Comment on the morphology of the red blood cells.
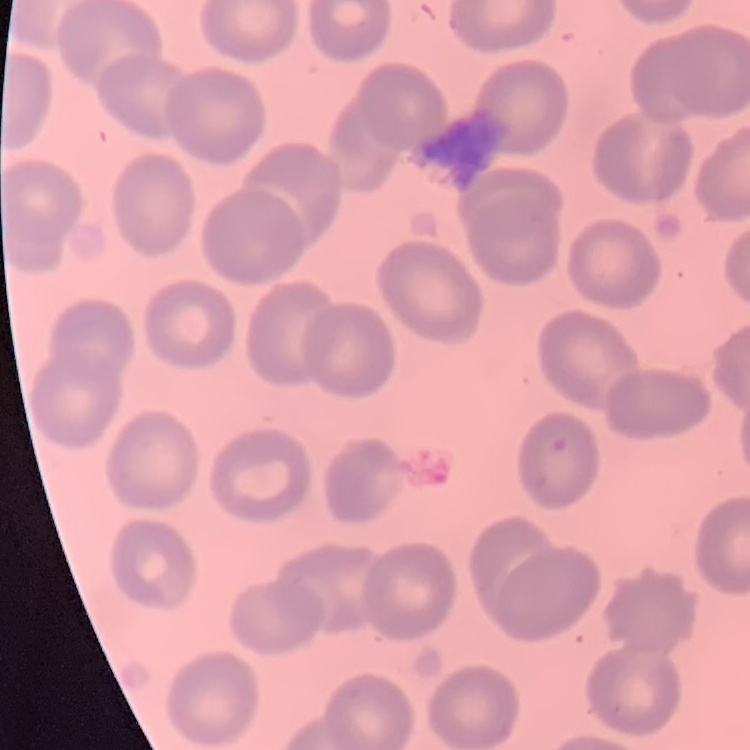

They show no rouleaux formation.

image type = one tile cut from a larger photomicrograph
stain = Field's or Giemsa
preparation = thin peripheral smear